Comment on the morphology of the erythrocytes.
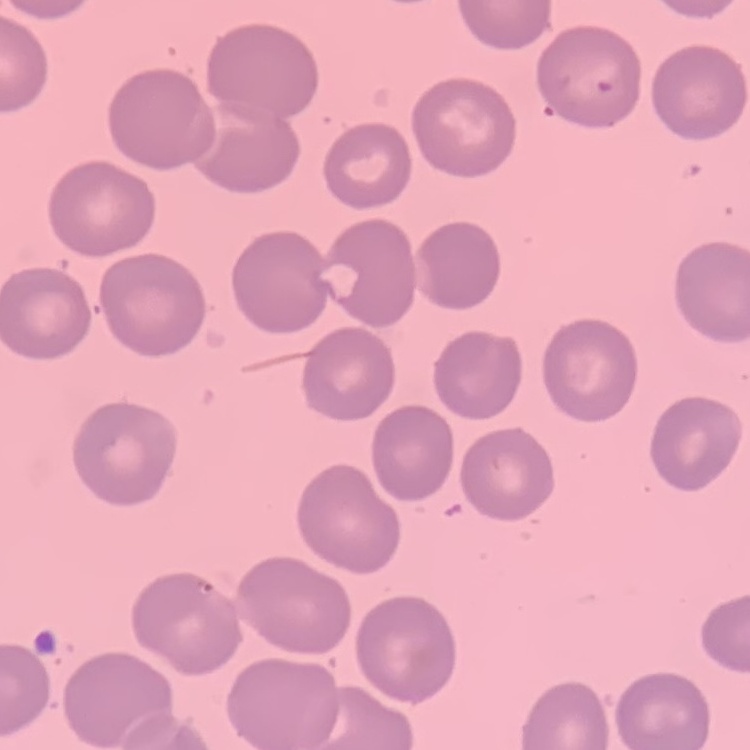
No rouleaux formation.

Summary:
  - Stain: Field's or Giemsa
  - Image type: one tile cut from a larger photomicrograph
  - Preparation: thin blood film